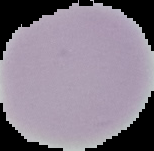
Image is 154×151 pixels. From a thin blood film. Malaria status: uninfected. Cell region segmented out of the field of view; the surrounding area is masked to black.